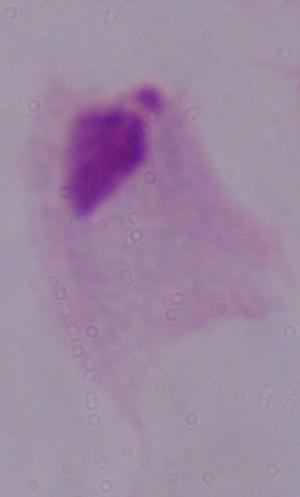
identification = trichomonad
magnification = 1000x
modality = micrograph